Draw a bounding box around every artifact (stain precipitate or debris).
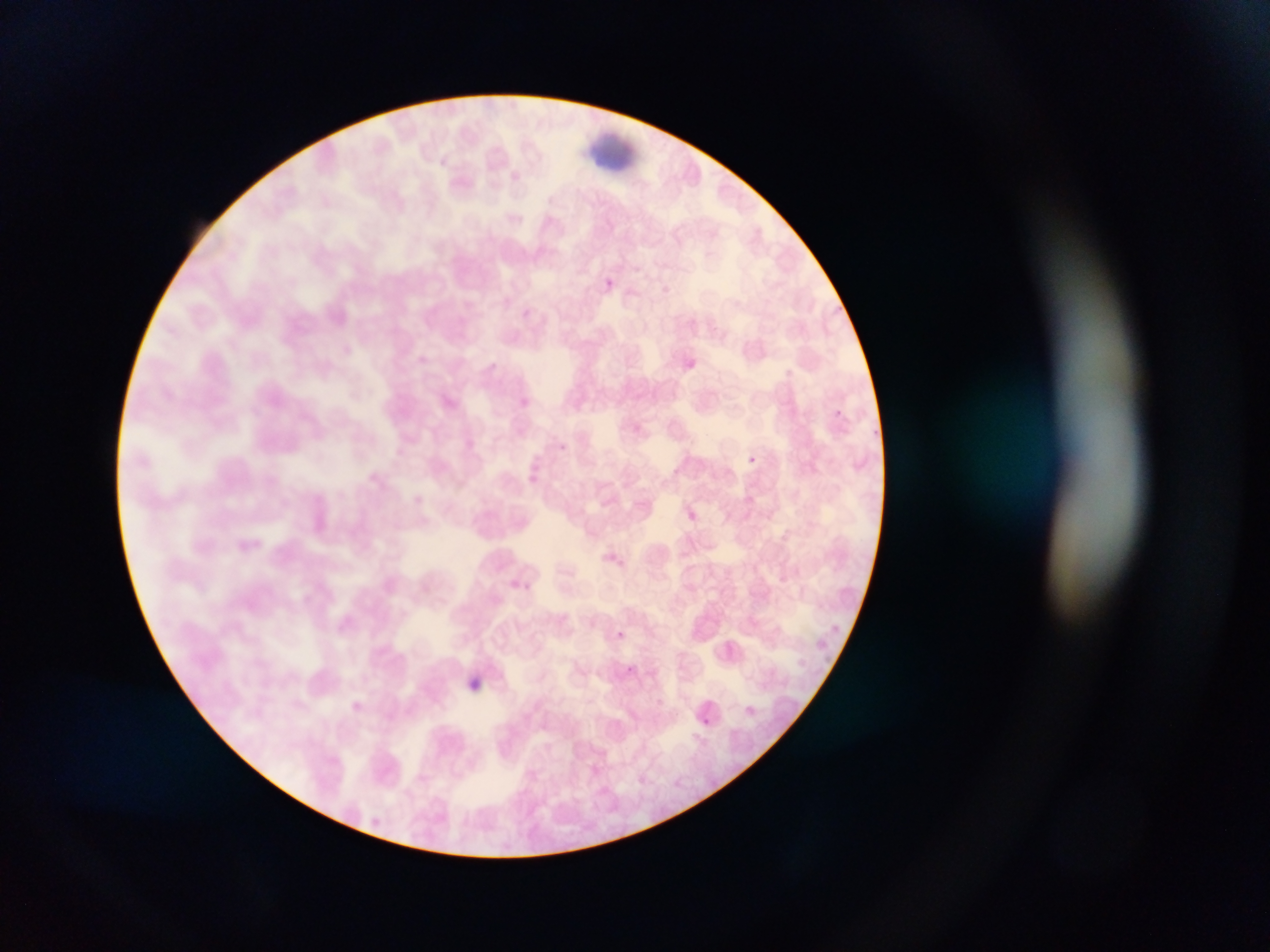

Approximate bounding boxes as [left, top, right, bottom] in pixels.
Artifacts (stain precipitate or debris): [591, 129, 639, 172].

Malaria parasite locations: [600, 276, 617, 292], [830, 406, 845, 420], [749, 453, 758, 465], [681, 506, 700, 525], [523, 576, 534, 595], [614, 630, 626, 637], [626, 661, 635, 669], [344, 696, 368, 718], [693, 713, 713, 731]. Thin blood smear. Image is 1270×952 pixels. Photographed through a microscope with a mobile-phone camera. Collected in Ghana. Single field of view.